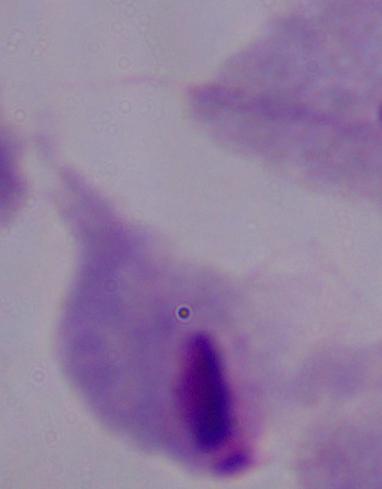
{
  "identification": "trichomonad",
  "modality": "micrograph",
  "magnification": "1000x"
}